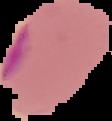
{
  "preparation": "thin blood film",
  "malaria_status": "parasitized",
  "image_size": "112×121 pixels",
  "image_type": "segmented cell region on a black background"
}